Identify the parasite.
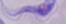
A trypanosome.

magnification = 1000x
modality = micrograph